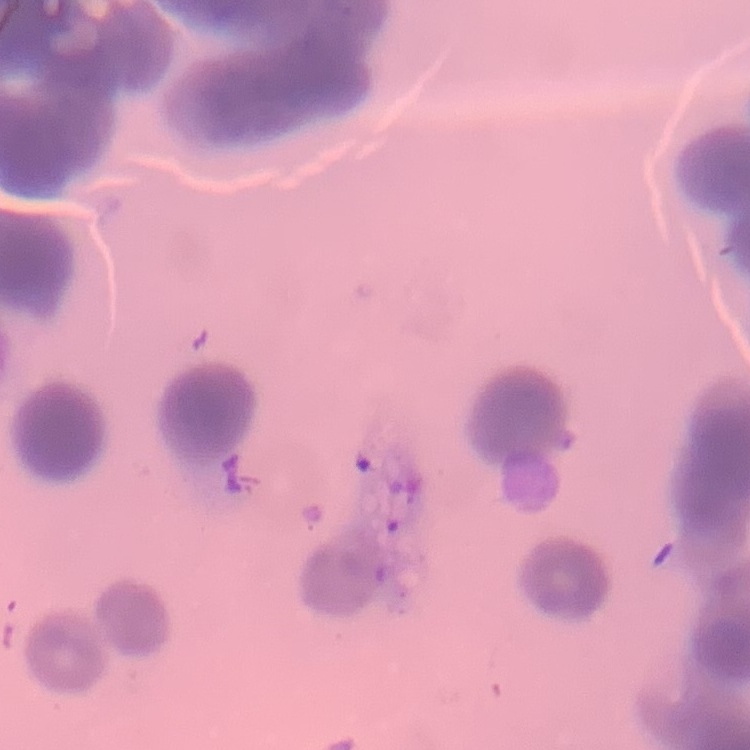
The erythrocytes exhibit rouleaux formation. Stained with either Field's or Giemsa. Thin peripheral smear. Square crop of a larger photomicrograph.